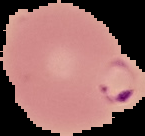
preparation = thin blood film
result = malaria parasites identified
image type = segmented cell region on a black background
image size = 145×136 pixels